Outline each Trypanosoma brucei.
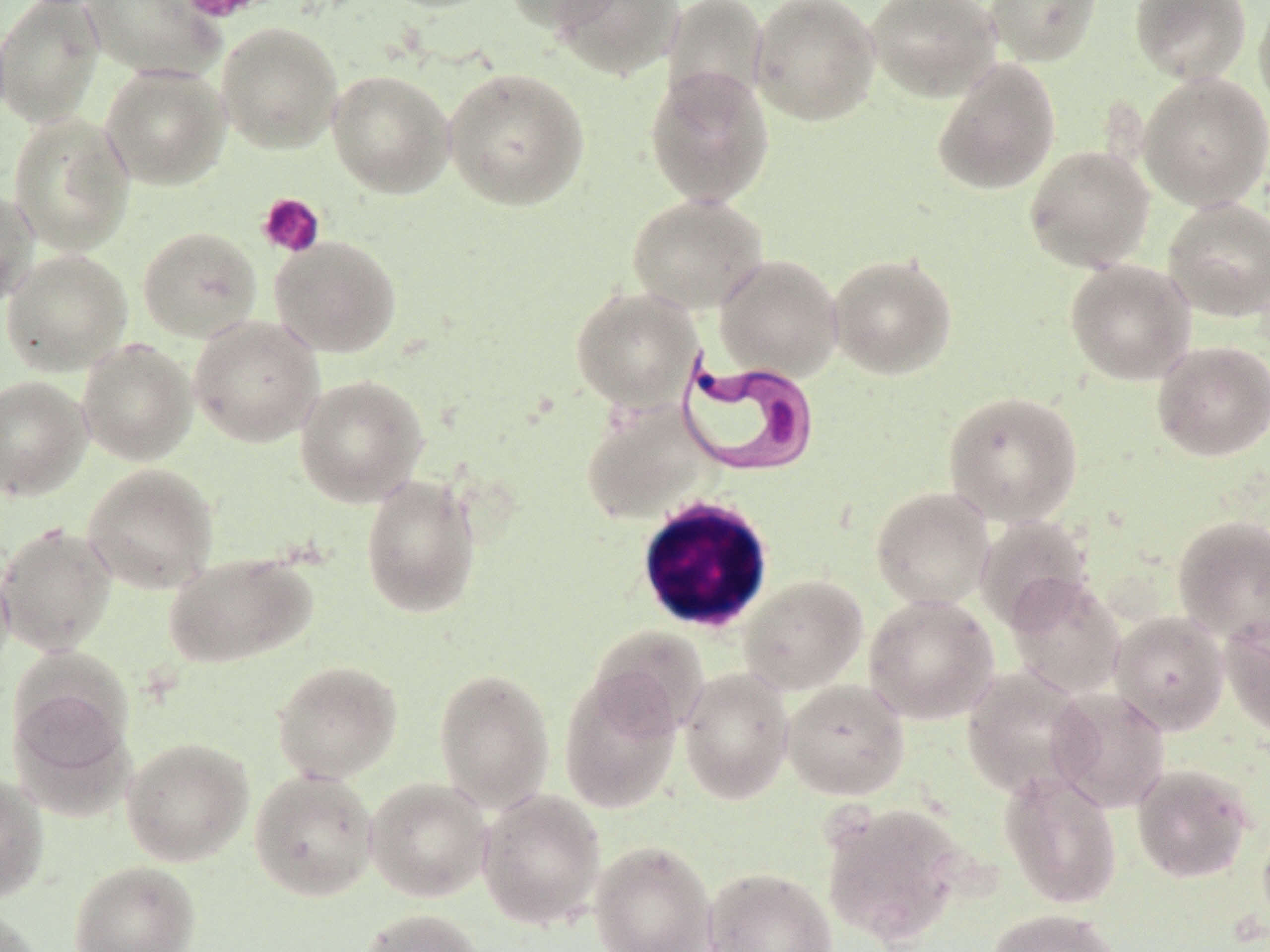

Approximate bounding boxes as named x1/y1/x2/y2 corners in pixels.
Trypanosoma brucei: (x1=675, y1=351, x2=821, y2=479).

Summary:
  - Uninfected red blood cell locations: (x1=0, y1=0, x2=105, y2=128), (x1=81, y1=0, x2=224, y2=81), (x1=378, y1=0, x2=502, y2=14), (x1=502, y1=0, x2=626, y2=32), (x1=550, y1=0, x2=683, y2=80), (x1=662, y1=0, x2=770, y2=113), (x1=749, y1=0, x2=881, y2=126), (x1=864, y1=0, x2=1002, y2=102), (x1=984, y1=0, x2=1102, y2=66), (x1=1129, y1=0, x2=1252, y2=85), (x1=1253, y1=0, x2=1270, y2=117), (x1=216, y1=21, x2=343, y2=154), (x1=932, y1=58, x2=1061, y2=196), (x1=100, y1=64, x2=231, y2=189), (x1=644, y1=66, x2=776, y2=208), (x1=443, y1=68, x2=590, y2=211), (x1=328, y1=69, x2=456, y2=198), (x1=1138, y1=73, x2=1270, y2=212), (x1=8, y1=112, x2=135, y2=257), (x1=1024, y1=144, x2=1155, y2=272), (x1=0, y1=186, x2=38, y2=308), (x1=627, y1=193, x2=768, y2=315), (x1=1162, y1=196, x2=1270, y2=321), (x1=138, y1=226, x2=262, y2=343), (x1=269, y1=235, x2=402, y2=358), (x1=1, y1=249, x2=133, y2=376), (x1=715, y1=253, x2=843, y2=381), (x1=827, y1=253, x2=958, y2=379), (x1=1064, y1=258, x2=1196, y2=385), (x1=570, y1=286, x2=702, y2=411), (x1=188, y1=316, x2=324, y2=447), (x1=77, y1=340, x2=197, y2=465), (x1=1151, y1=340, x2=1270, y2=462), (x1=294, y1=374, x2=429, y2=507), (x1=0, y1=375, x2=91, y2=501), (x1=942, y1=390, x2=1083, y2=526), (x1=581, y1=401, x2=714, y2=525), (x1=82, y1=463, x2=219, y2=594), (x1=360, y1=473, x2=482, y2=618), (x1=871, y1=486, x2=995, y2=610), (x1=1171, y1=514, x2=1270, y2=643), (x1=974, y1=515, x2=1092, y2=631), (x1=0, y1=523, x2=118, y2=656), (x1=0, y1=549, x2=13, y2=683), (x1=164, y1=552, x2=315, y2=668), (x1=738, y1=574, x2=868, y2=695), (x1=1005, y1=574, x2=1126, y2=699), (x1=863, y1=593, x2=1000, y2=725), (x1=1109, y1=611, x2=1230, y2=735), (x1=1220, y1=616, x2=1270, y2=738), (x1=588, y1=624, x2=709, y2=740), (x1=271, y1=660, x2=403, y2=783), (x1=678, y1=666, x2=795, y2=804), (x1=961, y1=666, x2=1095, y2=801), (x1=433, y1=668, x2=554, y2=812), (x1=558, y1=671, x2=682, y2=814), (x1=782, y1=678, x2=910, y2=801), (x1=7, y1=683, x2=133, y2=805), (x1=1048, y1=687, x2=1171, y2=813), (x1=121, y1=737, x2=254, y2=866), (x1=1131, y1=763, x2=1255, y2=884), (x1=249, y1=768, x2=379, y2=902), (x1=999, y1=768, x2=1123, y2=909), (x1=0, y1=772, x2=49, y2=904), (x1=364, y1=776, x2=492, y2=902), (x1=477, y1=788, x2=607, y2=931), (x1=820, y1=802, x2=968, y2=946), (x1=1257, y1=815, x2=1270, y2=935), (x1=589, y1=840, x2=716, y2=952), (x1=69, y1=860, x2=201, y2=952), (x1=703, y1=867, x2=838, y2=952), (x1=0, y1=906, x2=45, y2=952), (x1=356, y1=908, x2=486, y2=952), (x1=985, y1=908, x2=1122, y2=952)
  - White blood cell locations: (x1=634, y1=496, x2=775, y2=634)
  - Platelet locations: (x1=178, y1=0, x2=272, y2=23), (x1=257, y1=192, x2=326, y2=258)
  - Slide-level diagnosis: Trypanosoma brucei
  - Stain: May-Grünwald-Giemsa
  - Magnification: 1000x
  - Modality: optical microscopy
  - Image size: 1270×952 pixels
  - Preparation: thin blood smear
  - Field of view: single